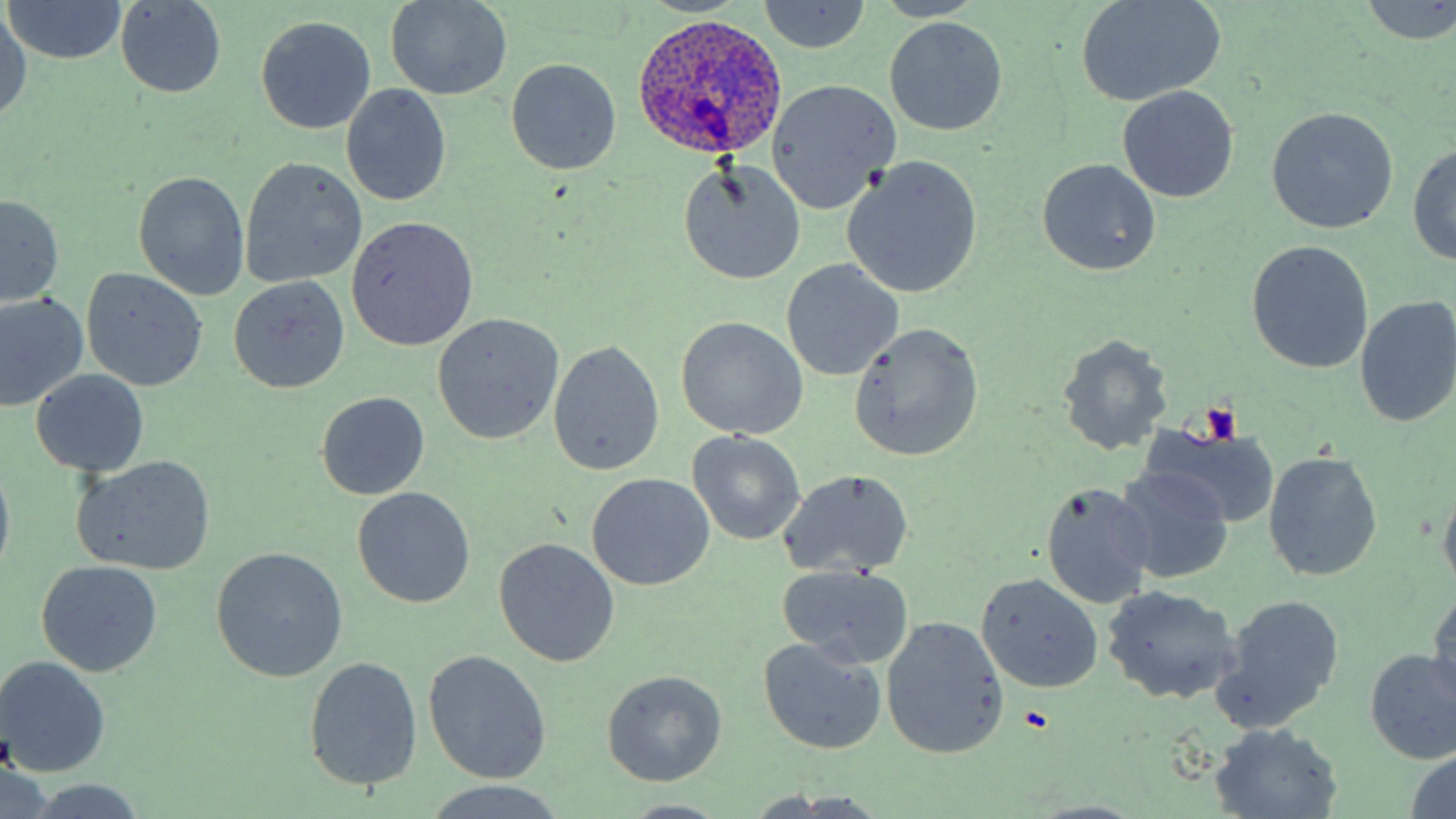 Approximate bounding boxes as named x1/y1/x2/y2 corners in pixels. Platelet locations: (x1=1202, y1=402, x2=1241, y2=445), (x1=1018, y1=704, x2=1051, y2=732). Uninfected red blood cell locations: (x1=3, y1=1, x2=129, y2=66), (x1=757, y1=1, x2=872, y2=54), (x1=1075, y1=1, x2=1228, y2=108), (x1=384, y1=2, x2=513, y2=100), (x1=115, y1=3, x2=227, y2=98), (x1=1358, y1=3, x2=1456, y2=43), (x1=0, y1=12, x2=31, y2=124), (x1=255, y1=15, x2=375, y2=134), (x1=884, y1=17, x2=1008, y2=137), (x1=506, y1=59, x2=622, y2=175), (x1=767, y1=81, x2=900, y2=215), (x1=341, y1=84, x2=452, y2=206), (x1=1117, y1=86, x2=1240, y2=202), (x1=1267, y1=107, x2=1398, y2=234), (x1=1408, y1=142, x2=1456, y2=265), (x1=238, y1=158, x2=367, y2=288), (x1=1036, y1=158, x2=1161, y2=276), (x1=842, y1=159, x2=982, y2=297), (x1=677, y1=160, x2=806, y2=285), (x1=133, y1=171, x2=249, y2=299), (x1=0, y1=195, x2=65, y2=309), (x1=344, y1=217, x2=478, y2=350), (x1=1247, y1=241, x2=1374, y2=374), (x1=781, y1=259, x2=902, y2=381), (x1=82, y1=267, x2=208, y2=393), (x1=229, y1=277, x2=350, y2=395), (x1=0, y1=294, x2=88, y2=411), (x1=1354, y1=296, x2=1456, y2=428), (x1=433, y1=314, x2=565, y2=445), (x1=674, y1=317, x2=809, y2=441), (x1=849, y1=322, x2=984, y2=463), (x1=1055, y1=334, x2=1173, y2=456), (x1=548, y1=340, x2=664, y2=476), (x1=29, y1=367, x2=151, y2=476), (x1=316, y1=392, x2=430, y2=501), (x1=1137, y1=422, x2=1280, y2=529), (x1=687, y1=431, x2=805, y2=545), (x1=1262, y1=452, x2=1383, y2=582), (x1=71, y1=456, x2=216, y2=575), (x1=0, y1=458, x2=16, y2=578), (x1=1112, y1=466, x2=1237, y2=585), (x1=777, y1=469, x2=915, y2=579), (x1=587, y1=473, x2=714, y2=591), (x1=1437, y1=479, x2=1456, y2=596), (x1=1040, y1=481, x2=1156, y2=608), (x1=351, y1=487, x2=476, y2=609), (x1=492, y1=537, x2=620, y2=668), (x1=211, y1=547, x2=347, y2=683), (x1=35, y1=559, x2=164, y2=677), (x1=776, y1=564, x2=915, y2=672), (x1=976, y1=572, x2=1104, y2=693), (x1=1101, y1=585, x2=1241, y2=705), (x1=1429, y1=589, x2=1456, y2=705), (x1=1214, y1=596, x2=1345, y2=729), (x1=881, y1=615, x2=1009, y2=761), (x1=756, y1=637, x2=887, y2=754), (x1=1363, y1=648, x2=1456, y2=765), (x1=422, y1=650, x2=552, y2=784), (x1=1, y1=655, x2=109, y2=777), (x1=303, y1=655, x2=423, y2=793), (x1=601, y1=670, x2=727, y2=786), (x1=1209, y1=726, x2=1343, y2=818), (x1=1407, y1=749, x2=1456, y2=816), (x1=21, y1=779, x2=151, y2=818), (x1=426, y1=781, x2=569, y2=817). Plasmodium ovale-infected red blood cell locations: (x1=630, y1=10, x2=790, y2=162). Slide-level diagnosis: Plasmodium ovale. May-Grünwald-Giemsa-stained preparation. Captured at 1000x magnification. One field of a larger specimen. Thin blood smear. Optical microscopy. Image is 1456×819 pixels.